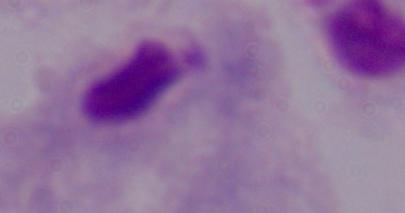 A trichomonad is shown. 1000x magnification. Micrograph.